Assess this cell for malaria.
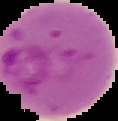
It is parasitized.

Summary:
  - Image type: segmented cell region with the area outside set to black
  - Preparation: thin blood film
  - Image size: 118×121 pixels